Point out each Plasmodium parasite.
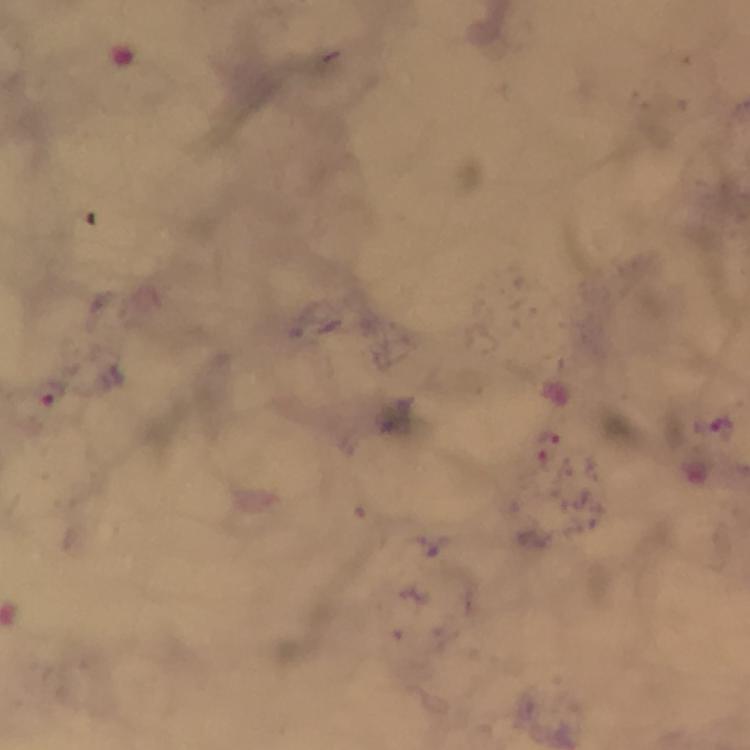
Approximate centers as {x, y} in pixels.
Plasmodium parasites: {721, 424}.

cropped from = one field of view
capture = smartphone photograph through a microscope
magnification = 100x
context = from a malaria diagnostic workup
immersion oil = used
preparation = thick blood film
stain = Giemsa
image size = 750×750 pixels